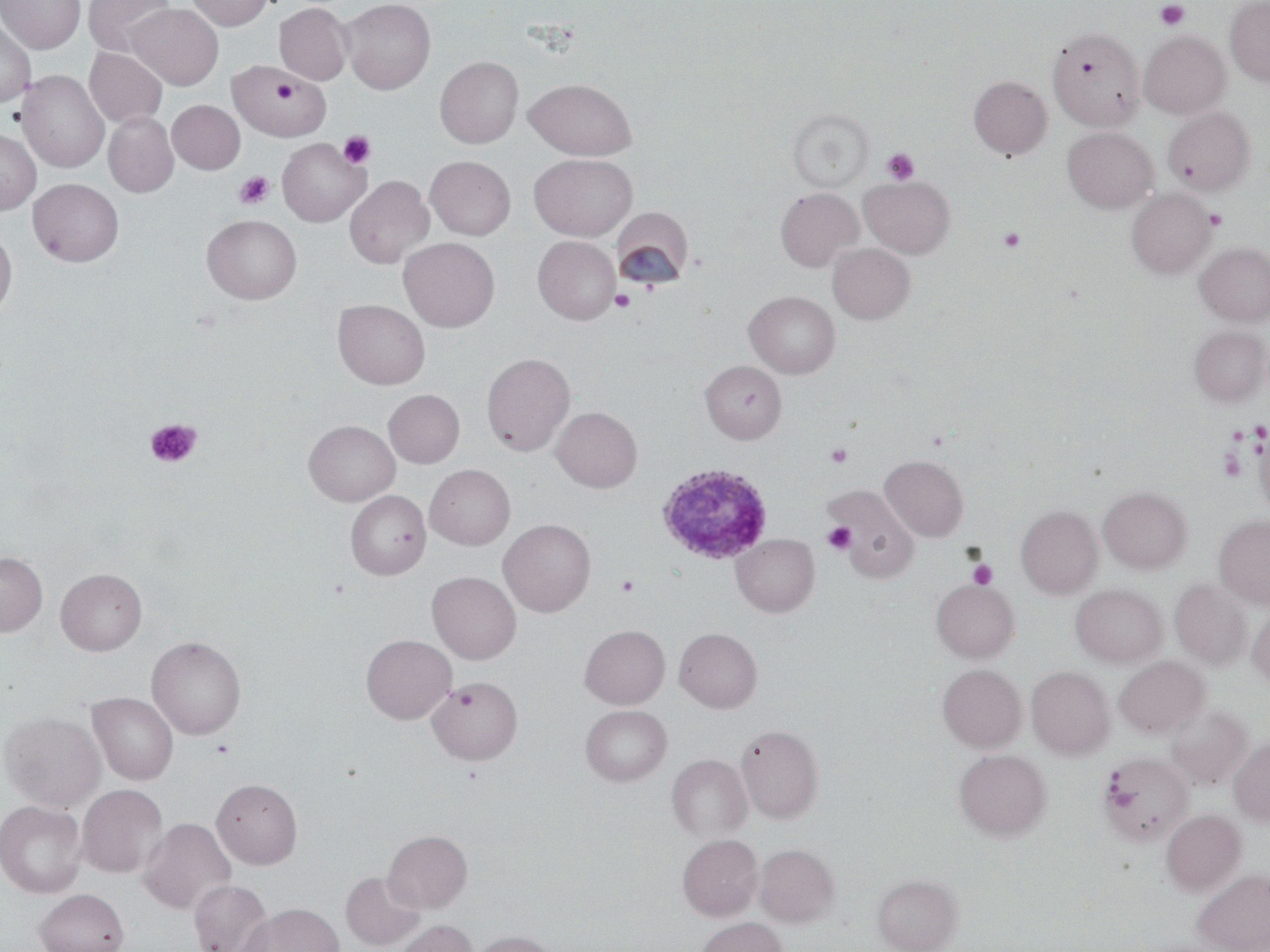
Summary:
  - Coordinate format: approximate bounding boxes as (x1, y1, x2, y2) in pixels
  - Platelet locations: (1155, 1, 1190, 29), (272, 78, 298, 105), (338, 131, 375, 169), (881, 148, 919, 185), (235, 171, 273, 209), (1205, 209, 1226, 229), (998, 227, 1025, 252), (610, 289, 636, 311), (144, 418, 202, 468), (825, 444, 852, 468), (1218, 447, 1246, 483), (823, 522, 856, 554), (969, 560, 997, 589), (615, 574, 639, 596), (211, 739, 234, 758)
  - Plasmodium ovale-infected red blood cell locations: (656, 463, 772, 564)
  - Uninfected red blood cell locations: (0, 0, 85, 53), (84, 0, 177, 57), (187, 0, 272, 30), (341, 0, 435, 94), (1224, 0, 1270, 85), (275, 2, 353, 85), (126, 3, 223, 89), (0, 18, 36, 106), (1047, 27, 1145, 131), (1138, 30, 1231, 119), (85, 47, 167, 128), (435, 56, 523, 148), (227, 61, 330, 142), (17, 70, 109, 173), (968, 75, 1052, 159), (524, 78, 637, 160), (167, 100, 245, 174), (1163, 106, 1255, 196), (787, 108, 874, 192), (103, 112, 179, 197), (1062, 126, 1158, 214), (0, 129, 41, 214), (277, 137, 369, 226), (529, 153, 637, 241), (425, 156, 516, 240), (344, 175, 434, 269), (859, 176, 955, 258), (28, 178, 124, 266), (775, 188, 863, 271), (1126, 188, 1215, 278), (611, 210, 694, 290), (202, 214, 302, 304), (0, 230, 17, 319), (533, 236, 620, 324), (398, 237, 500, 332), (1195, 242, 1270, 325), (827, 243, 914, 324), (744, 291, 840, 379), (333, 299, 430, 390), (1188, 325, 1269, 407), (481, 352, 575, 456), (700, 359, 787, 444), (383, 389, 464, 468), (551, 406, 642, 493), (304, 420, 400, 506), (1252, 420, 1270, 520), (880, 454, 969, 541), (425, 464, 515, 550), (1098, 485, 1192, 573), (827, 486, 918, 582), (345, 490, 431, 579), (1016, 505, 1103, 598), (1214, 514, 1270, 609), (498, 518, 596, 617), (731, 533, 819, 617), (0, 552, 48, 636), (56, 568, 147, 655), (427, 571, 521, 664), (1170, 578, 1253, 669), (931, 579, 1019, 663), (1070, 583, 1167, 668), (1247, 605, 1270, 687), (579, 624, 670, 708), (674, 627, 763, 713), (360, 634, 456, 724), (146, 635, 246, 740), (1114, 656, 1209, 739), (937, 664, 1026, 752), (1026, 666, 1114, 759), (426, 676, 523, 765), (87, 692, 178, 785), (1165, 703, 1253, 791), (580, 704, 672, 786), (1, 711, 105, 812), (735, 723, 824, 823), (1229, 739, 1270, 826), (954, 749, 1052, 841), (1097, 752, 1194, 845), (667, 754, 752, 841), (211, 777, 303, 869), (76, 784, 168, 878), (0, 800, 87, 898), (1161, 809, 1246, 895), (138, 817, 236, 915), (383, 829, 472, 913), (677, 833, 763, 921), (754, 843, 840, 927), (1192, 870, 1270, 951), (341, 871, 425, 950), (872, 873, 962, 952), (189, 880, 273, 952), (34, 888, 129, 952), (241, 904, 343, 952), (695, 917, 788, 952), (395, 919, 478, 952), (471, 930, 556, 952)
  - Slide-level diagnosis: Plasmodium ovale
  - Stain: May-Grünwald-Giemsa
  - Modality: optical microscopy
  - Preparation: thin blood film
  - Image size: 1270×952 pixels
  - Field of view: single
  - Magnification: 1000x